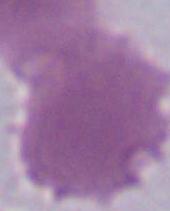

Summary:
  - Modality: micrograph
  - Magnification: 1000x
  - Identification: red blood cell